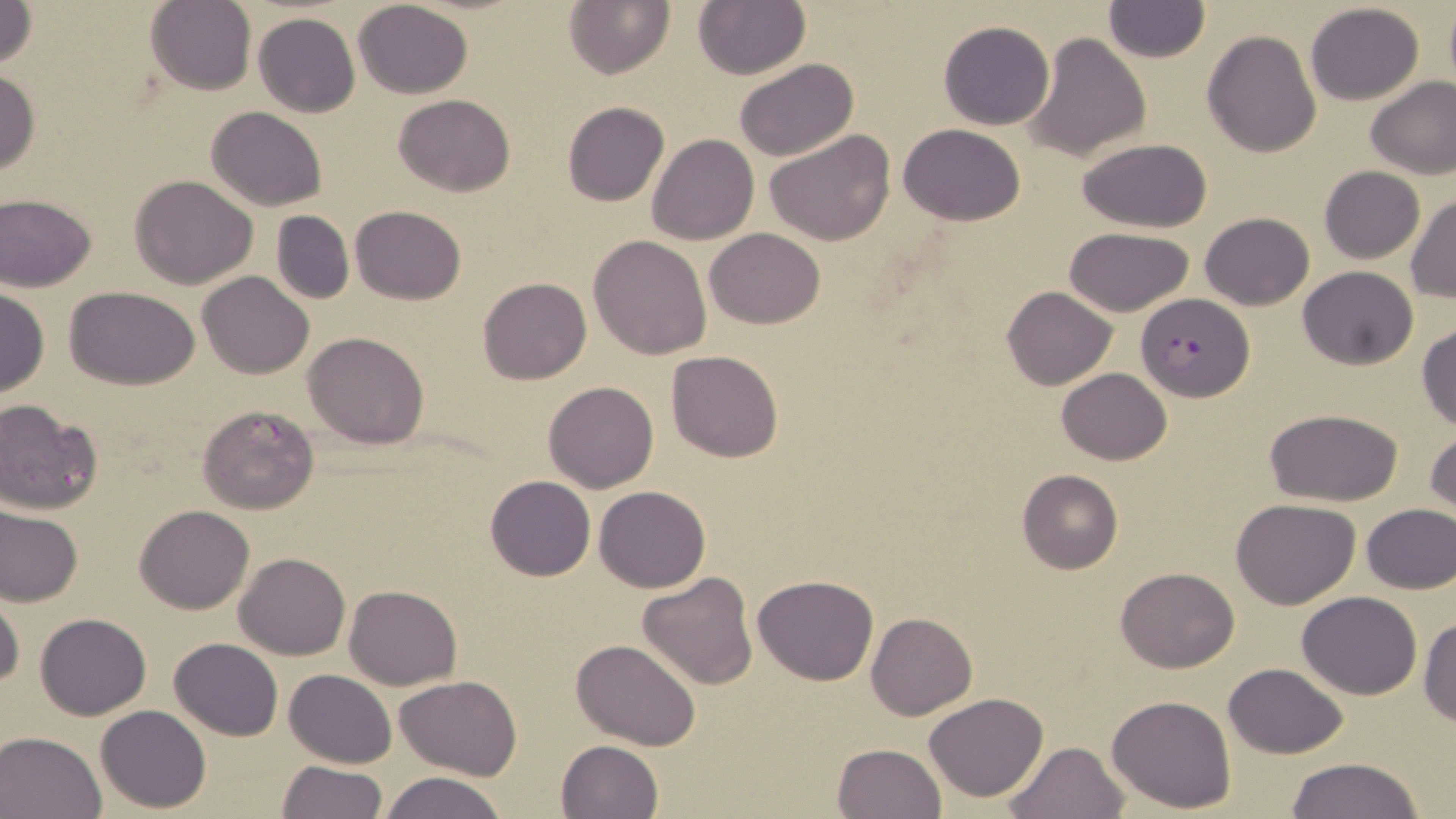

Approximate bounding boxes as named x1/y1/x2/y2 corners in pixels. Uninfected red blood cell locations: (x1=0, y1=0, x2=39, y2=68), (x1=564, y1=0, x2=675, y2=79), (x1=145, y1=1, x2=256, y2=94), (x1=352, y1=1, x2=473, y2=98), (x1=694, y1=2, x2=809, y2=78), (x1=1102, y1=3, x2=1210, y2=63), (x1=1305, y1=3, x2=1426, y2=105), (x1=1443, y1=3, x2=1456, y2=91), (x1=254, y1=13, x2=360, y2=117), (x1=939, y1=21, x2=1054, y2=129), (x1=1202, y1=29, x2=1322, y2=158), (x1=1023, y1=32, x2=1150, y2=162), (x1=733, y1=58, x2=856, y2=162), (x1=0, y1=70, x2=41, y2=175), (x1=1365, y1=74, x2=1456, y2=179), (x1=392, y1=93, x2=514, y2=197), (x1=563, y1=101, x2=669, y2=207), (x1=206, y1=107, x2=327, y2=211), (x1=898, y1=124, x2=1025, y2=225), (x1=764, y1=129, x2=895, y2=244), (x1=646, y1=133, x2=759, y2=244), (x1=1078, y1=139, x2=1212, y2=232), (x1=1319, y1=165, x2=1425, y2=263), (x1=130, y1=175, x2=259, y2=289), (x1=0, y1=193, x2=97, y2=290), (x1=1407, y1=195, x2=1455, y2=302), (x1=352, y1=205, x2=466, y2=304), (x1=271, y1=211, x2=355, y2=304), (x1=1199, y1=212, x2=1314, y2=311), (x1=1063, y1=227, x2=1197, y2=317), (x1=704, y1=228, x2=827, y2=328), (x1=588, y1=234, x2=712, y2=360), (x1=1297, y1=266, x2=1418, y2=369), (x1=198, y1=271, x2=314, y2=379), (x1=478, y1=277, x2=591, y2=384), (x1=1003, y1=286, x2=1117, y2=389), (x1=65, y1=287, x2=199, y2=389), (x1=0, y1=289, x2=49, y2=396), (x1=1416, y1=324, x2=1456, y2=433), (x1=302, y1=331, x2=430, y2=450), (x1=665, y1=350, x2=783, y2=462), (x1=1057, y1=368, x2=1171, y2=464), (x1=542, y1=382, x2=660, y2=494), (x1=0, y1=399, x2=102, y2=514), (x1=195, y1=403, x2=320, y2=515), (x1=1265, y1=407, x2=1402, y2=505), (x1=1425, y1=428, x2=1456, y2=525), (x1=1017, y1=469, x2=1124, y2=574), (x1=485, y1=475, x2=596, y2=581), (x1=594, y1=485, x2=709, y2=593), (x1=1230, y1=497, x2=1360, y2=608), (x1=1360, y1=503, x2=1456, y2=593), (x1=135, y1=504, x2=254, y2=614), (x1=0, y1=508, x2=82, y2=608), (x1=235, y1=552, x2=350, y2=660), (x1=1116, y1=566, x2=1239, y2=673), (x1=636, y1=572, x2=759, y2=692), (x1=753, y1=574, x2=879, y2=685), (x1=344, y1=584, x2=463, y2=690), (x1=0, y1=589, x2=24, y2=690), (x1=1296, y1=590, x2=1421, y2=698), (x1=35, y1=612, x2=151, y2=718), (x1=866, y1=612, x2=977, y2=719), (x1=1418, y1=617, x2=1456, y2=727), (x1=170, y1=637, x2=284, y2=741), (x1=573, y1=639, x2=699, y2=751), (x1=1223, y1=663, x2=1348, y2=758), (x1=284, y1=669, x2=396, y2=767), (x1=395, y1=675, x2=520, y2=779), (x1=924, y1=691, x2=1049, y2=803), (x1=1106, y1=694, x2=1237, y2=811), (x1=96, y1=705, x2=210, y2=812), (x1=0, y1=729, x2=106, y2=819), (x1=555, y1=739, x2=663, y2=819), (x1=1004, y1=741, x2=1128, y2=819), (x1=831, y1=743, x2=944, y2=819), (x1=1284, y1=757, x2=1428, y2=818), (x1=277, y1=760, x2=386, y2=818), (x1=380, y1=772, x2=510, y2=819). Plasmodium falciparum-infected red blood cell locations: (x1=1135, y1=294, x2=1253, y2=400). Slide-level diagnosis: Plasmodium falciparum. Optical microscopy. May-Grünwald-Giemsa-stained preparation. 1000x magnification. Single field of view. Thin blood smear. Image is 1456×819 pixels.